Give the position of every Plasmodium parasite visible.
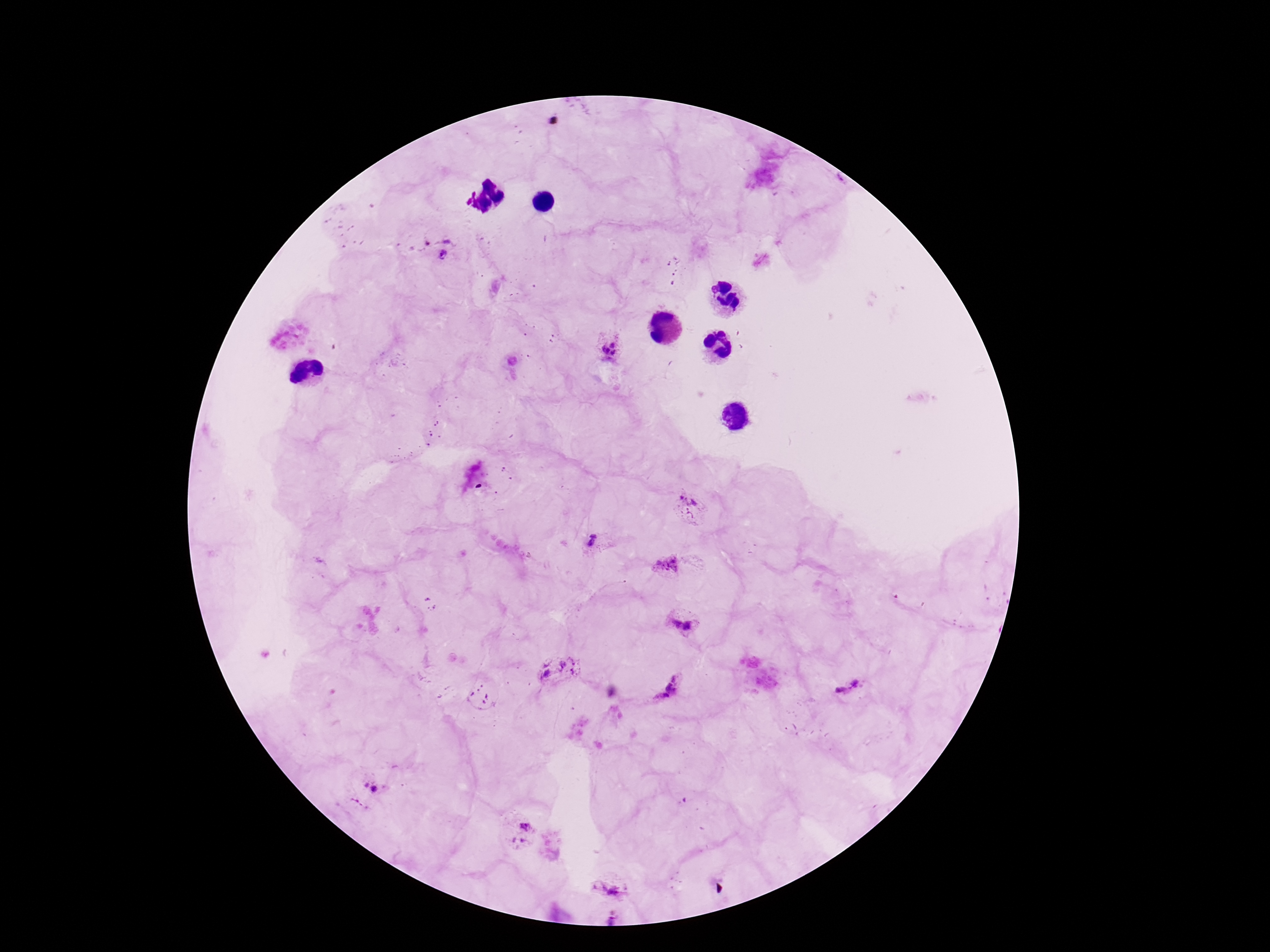
Approximate object centers, in pixels from the top-left corner.
Plasmodium parasites: (x=436, y=246), (x=610, y=351), (x=688, y=509), (x=595, y=544), (x=668, y=565), (x=681, y=621), (x=557, y=674), (x=849, y=687), (x=667, y=688), (x=372, y=789), (x=518, y=831), (x=612, y=881).

Summary:
  - Stain: Giemsa
  - Capture: smartphone camera through the microscope eyepiece
  - Preparation: thick blood smear
  - Magnification: 100x
  - Image size: 1270×952 pixels
  - Field of view: single
  - Patient malaria status: infected